Report the malaria status of this cell.
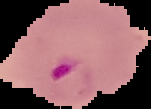

Parasitized.

Summary:
  - Preparation: thin blood smear
  - Image type: cell region segmented out of the field of view; surrounding area masked to black
  - Image size: 151×109 pixels